Report the malaria status of this cell.
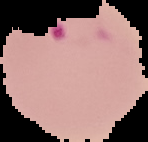
Parasitized.

image type = cell region segmented out of the field of view; surrounding area masked to black
preparation = thin blood film
image size = 148×142 pixels